Outline each Plasmodium malariae-infected red blood cell.
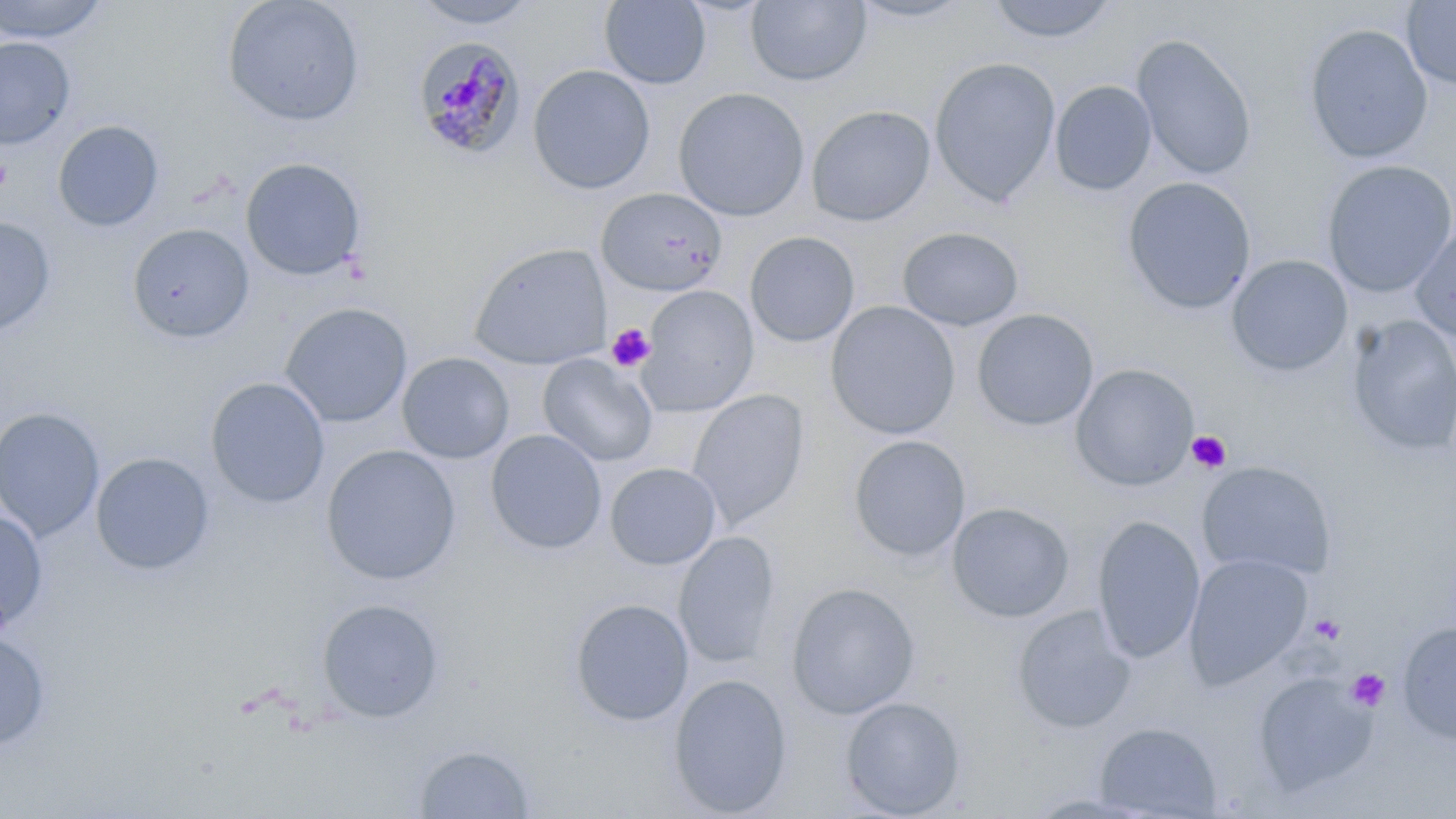

Approximate bounding boxes as (x1, y1, x2, y2) in pixels.
Plasmodium malariae-infected red blood cells: (411, 37, 526, 160).

Summary:
  - Uninfected red blood cell locations: (0, 0, 111, 44), (222, 0, 365, 127), (409, 0, 541, 29), (847, 0, 978, 24), (985, 0, 1119, 45), (599, 1, 712, 89), (745, 1, 872, 87), (1401, 1, 1456, 90), (1302, 23, 1434, 164), (1131, 33, 1258, 181), (0, 37, 75, 149), (929, 57, 1061, 207), (527, 64, 655, 194), (1050, 80, 1157, 195), (673, 88, 810, 221), (806, 105, 936, 226), (52, 121, 164, 231), (240, 157, 366, 281), (1321, 160, 1456, 297), (1122, 177, 1256, 314), (596, 188, 728, 296), (0, 216, 56, 335), (1409, 221, 1456, 344), (127, 223, 254, 343), (897, 227, 1024, 331), (745, 231, 860, 346), (469, 242, 611, 370), (1226, 254, 1354, 376), (637, 285, 759, 416), (825, 301, 961, 440), (280, 302, 413, 427), (971, 308, 1099, 431), (1346, 315, 1456, 457), (397, 352, 515, 464), (538, 354, 658, 467), (1069, 363, 1199, 491), (206, 377, 329, 508), (687, 389, 810, 531), (0, 407, 105, 541), (485, 429, 607, 555), (848, 435, 971, 562), (321, 444, 461, 585), (90, 452, 215, 575), (1196, 461, 1337, 580), (605, 462, 721, 569), (946, 502, 1075, 623), (0, 512, 48, 632), (1091, 515, 1205, 663), (673, 531, 780, 668), (1184, 554, 1313, 689), (785, 582, 921, 719), (316, 598, 445, 722), (569, 598, 694, 726), (1012, 606, 1136, 734), (1396, 621, 1456, 746), (0, 630, 51, 752), (1252, 672, 1376, 794), (667, 673, 793, 817), (840, 696, 966, 818), (1094, 722, 1222, 818), (414, 744, 536, 818)
  - Platelet locations: (0, 154, 13, 194), (606, 322, 655, 373), (1186, 430, 1231, 473), (1309, 613, 1346, 645), (1346, 668, 1390, 712)
  - Slide-level diagnosis: Plasmodium malariae
  - Image size: 1456×819 pixels
  - Field of view: one of a larger specimen
  - Preparation: thin blood smear
  - Modality: optical microscopy
  - Stain: May-Grünwald-Giemsa
  - Magnification: 1000x